Outline each Plasmodium vivax-infected red blood cell.
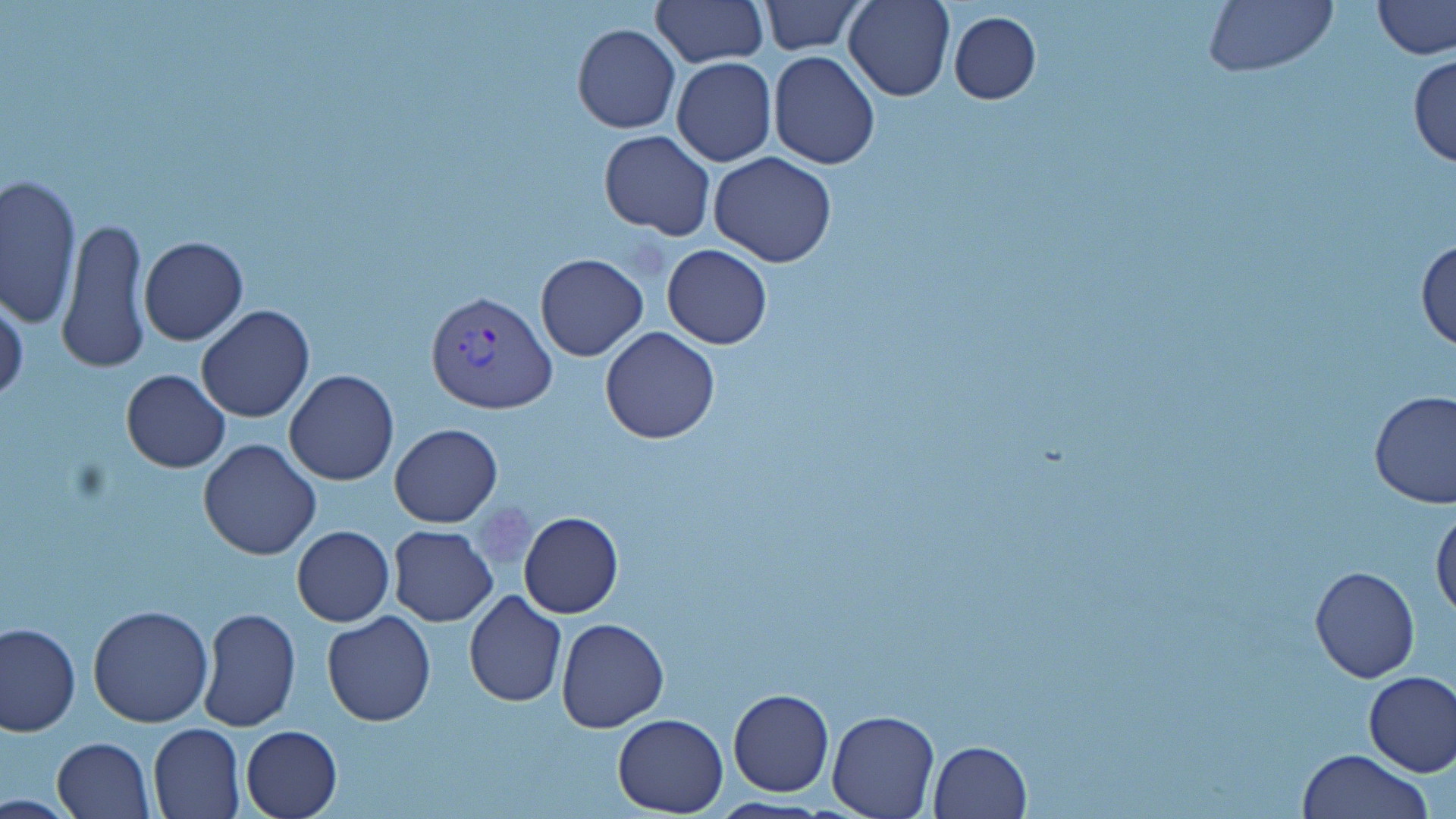
Approximate bounding boxes as [x1, y1, x2, y2] in pixels.
Plasmodium vivax-infected red blood cells: [427, 288, 558, 413].

Platelet locations: [467, 497, 539, 577]. Uninfected red blood cell locations: [650, 0, 766, 67], [759, 0, 866, 54], [844, 0, 956, 103], [1200, 0, 1338, 75], [1371, 0, 1455, 60], [949, 12, 1041, 104], [572, 23, 680, 133], [768, 50, 880, 169], [1410, 53, 1456, 169], [671, 58, 777, 167], [599, 128, 716, 240], [708, 152, 838, 268], [1, 174, 81, 328], [57, 218, 151, 373], [140, 235, 248, 345], [1415, 236, 1456, 353], [661, 244, 772, 350], [534, 252, 648, 361], [0, 295, 28, 406], [195, 305, 315, 423], [599, 326, 721, 444], [121, 369, 230, 473], [283, 369, 399, 486], [1370, 391, 1456, 511], [390, 423, 502, 527], [198, 438, 321, 559], [1429, 501, 1455, 622], [518, 511, 623, 618], [292, 525, 395, 626], [389, 526, 497, 626], [1310, 565, 1420, 683], [463, 592, 567, 708], [462, 604, 668, 717], [87, 605, 214, 727], [199, 608, 300, 731], [321, 611, 436, 727], [556, 617, 668, 732], [1, 622, 79, 737], [1363, 671, 1456, 777], [728, 688, 834, 797], [1322, 691, 1456, 816], [826, 708, 939, 818], [612, 713, 727, 817], [147, 723, 243, 818], [241, 724, 343, 818], [50, 737, 156, 818], [928, 740, 1032, 818], [1299, 748, 1434, 819]. Slide-level diagnosis: Plasmodium vivax. Thin blood smear. Image is 1456×819 pixels. 1000x magnification. May-Grünwald-Giemsa-stained preparation. Light microscopy. One field of a larger specimen.